State which parasite is depicted.
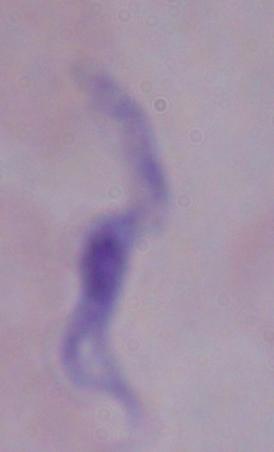

This is a trypanosome.

1000x magnification. Photomicrograph.